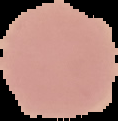
result = no malaria parasites detected
image size = 118×121 pixels
preparation = thin blood film
image type = cell region segmented out of the field of view; surrounding area masked to black